State which parasite is depicted.
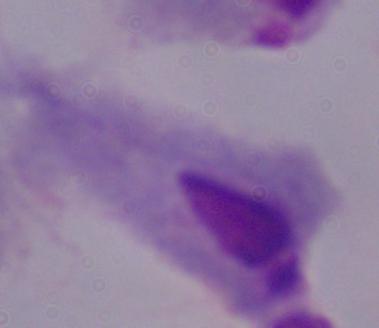
This is a trichomonad.

Summary:
  - Magnification: 1000x
  - Modality: photomicrograph